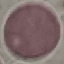

malaria_status: uninfected
image_type: cell patch, automatically extracted from a larger field of view and resized to 64 × 64 pixels
stain: Giemsa
preparation: thin smear
capture: smartphone through the microscope eyepiece